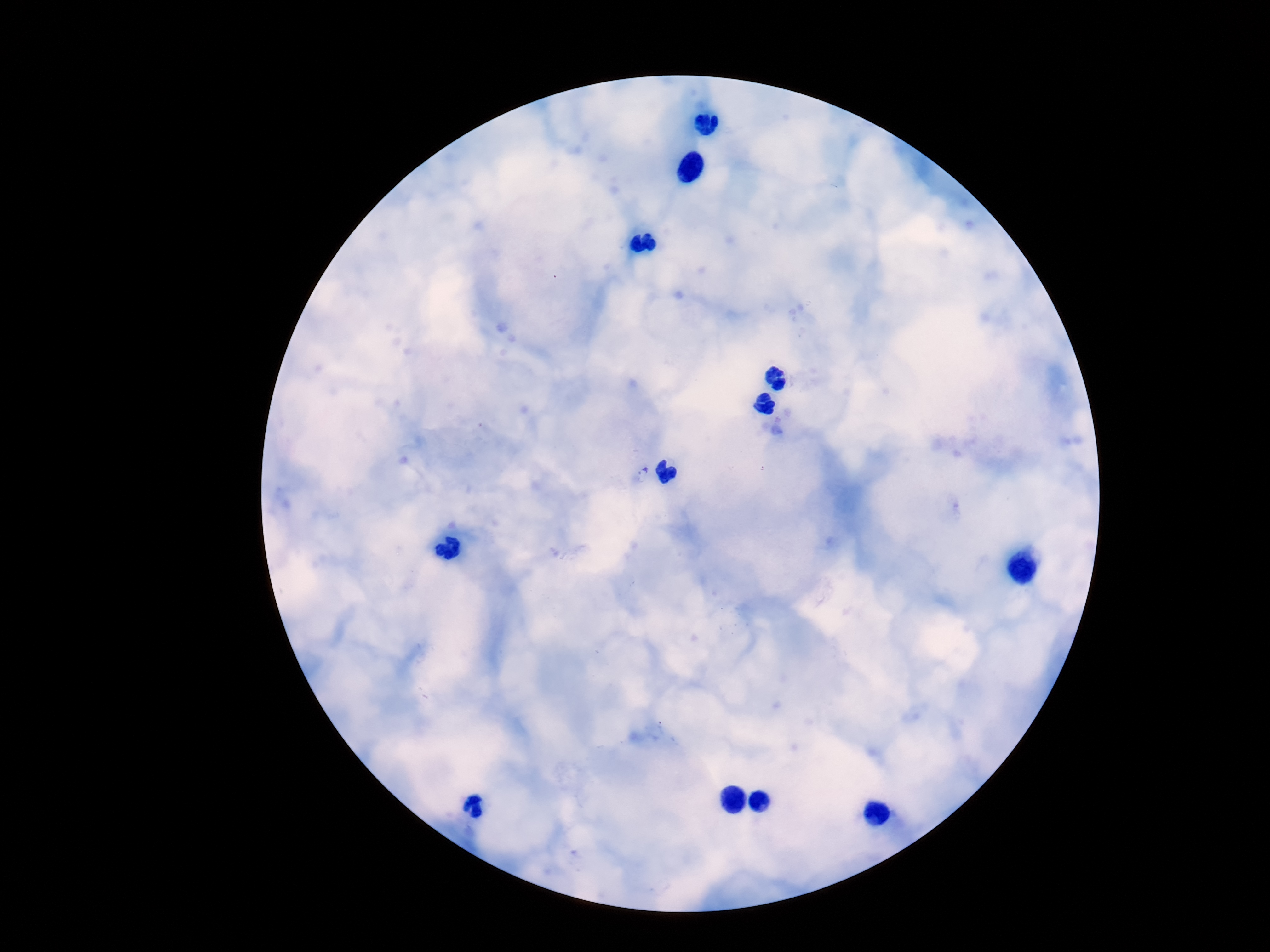
plasmodium_parasite_locations: 'approximate centers as [x, y] in pixels: [643, 474]'
preparation: thick blood smear
capture: smartphone camera through the microscope eyepiece
image_size: 1270×952 pixels
field_of_view: one from this slide
magnification: 100x
stain: Giemsa
patient_malaria_status: infected